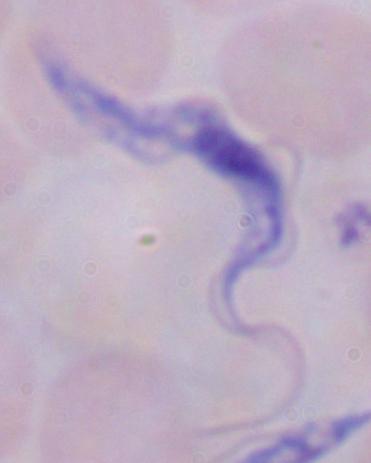
Summary:
  - Modality: photomicrograph
  - Identification: trypanosome
  - Magnification: 1000x